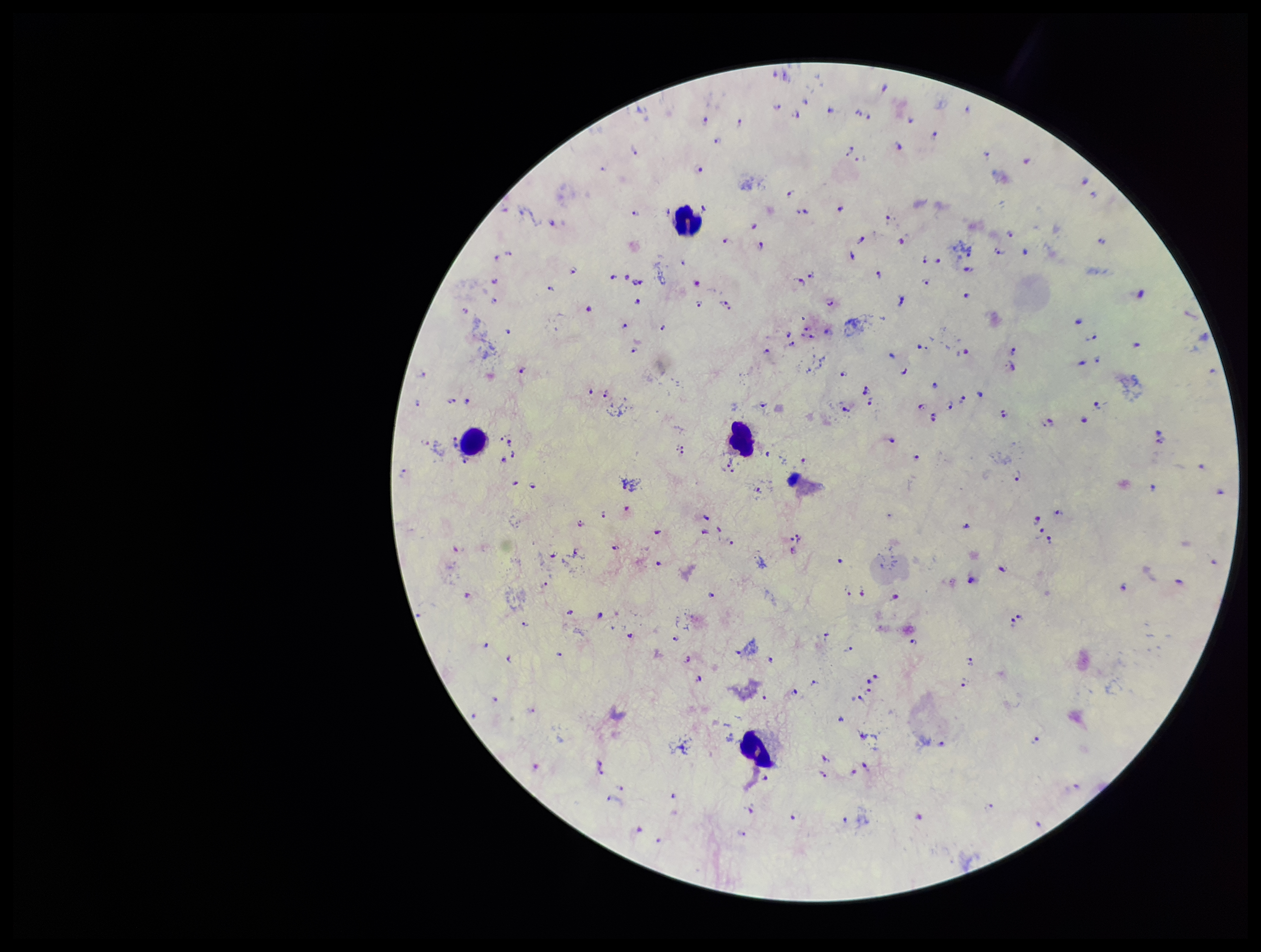
Preparation: thick smear. Giemsa stain. Smartphone photograph taken through the eyepiece of a microscope. One field from this slide. Species reported for this patient: Plasmodium falciparum. Leukocyte count: 4. Plasmodium parasites: detected. Image is 1261×952 pixels. Patient malaria status: positive. Parasite count: 139.